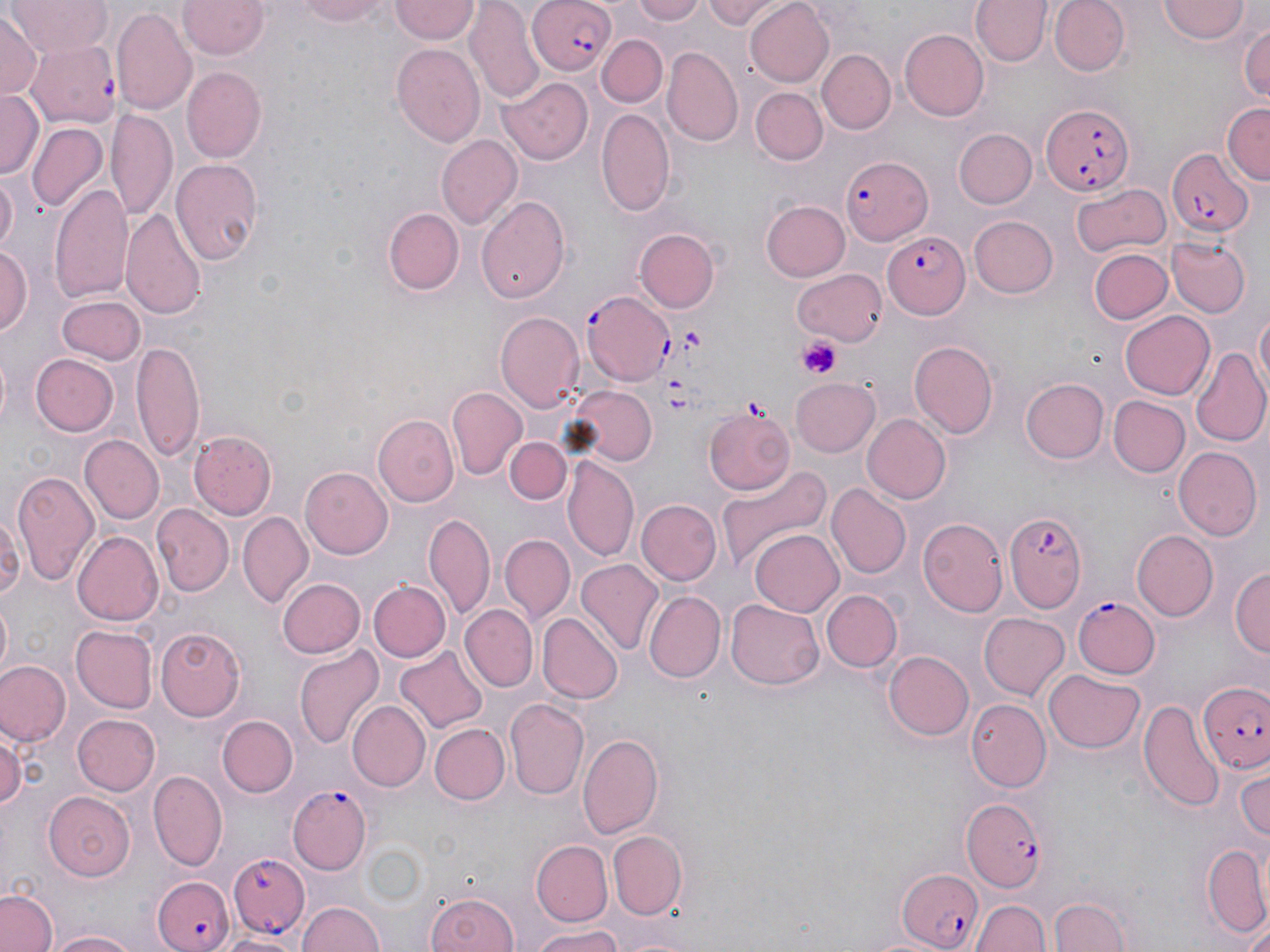

slide-level diagnosis = Plasmodium falciparum
preparation = thin blood smear
stain = May-Grünwald-Giemsa
platelet locations = approximate bounding boxes as [x1, y1, x2, y2] in pixels: [680, 325, 710, 356], [798, 338, 841, 378], [740, 394, 769, 415]
modality = light microscopy
uninfected red blood cell locations = approximate bounding boxes as [x1, y1, x2, y2] in pixels: [7, 0, 112, 59], [178, 0, 268, 58], [291, 0, 397, 26], [631, 0, 706, 24], [703, 0, 778, 31], [969, 0, 1049, 67], [1049, 0, 1129, 74], [390, 1, 479, 43], [743, 1, 835, 88], [1158, 1, 1248, 44], [465, 5, 545, 101], [111, 9, 196, 116], [0, 11, 41, 100], [1238, 18, 1270, 107], [898, 28, 989, 121], [596, 34, 667, 107], [390, 40, 484, 144], [663, 48, 743, 145], [819, 50, 895, 134], [183, 66, 265, 163], [499, 76, 592, 164], [750, 87, 827, 166], [1, 91, 42, 177], [1222, 103, 1270, 184], [595, 106, 676, 218], [108, 108, 177, 222], [26, 122, 107, 214], [952, 129, 1036, 209], [438, 135, 522, 228], [170, 159, 263, 266], [1, 174, 18, 260], [1071, 181, 1171, 262], [49, 183, 134, 302], [476, 193, 571, 305], [761, 200, 851, 281], [122, 207, 207, 322], [383, 208, 463, 295], [970, 216, 1059, 298], [634, 228, 718, 313], [1169, 235, 1251, 316], [0, 244, 31, 340], [1090, 248, 1172, 325], [792, 268, 888, 344], [57, 298, 146, 365], [495, 309, 584, 410], [1254, 309, 1270, 401], [1121, 312, 1215, 399], [132, 336, 205, 465], [910, 340, 998, 437], [1192, 346, 1270, 445], [29, 353, 119, 437], [791, 376, 881, 455], [1023, 378, 1108, 463], [566, 386, 657, 469], [447, 389, 526, 480], [1108, 396, 1189, 477], [704, 407, 796, 496], [375, 413, 457, 506], [863, 415, 950, 502], [189, 430, 277, 517], [79, 434, 164, 524], [504, 437, 571, 505], [1173, 446, 1260, 539], [562, 454, 638, 563], [717, 465, 833, 569], [301, 466, 394, 557], [11, 468, 99, 583], [826, 485, 909, 579], [637, 501, 719, 584], [152, 505, 233, 595], [0, 510, 21, 605], [237, 513, 313, 606], [425, 515, 494, 616], [917, 518, 1007, 617], [750, 529, 844, 617], [73, 530, 164, 625], [1132, 531, 1218, 620], [499, 535, 573, 620], [576, 559, 664, 657], [1231, 565, 1269, 661], [277, 577, 366, 659], [369, 581, 449, 662], [646, 589, 726, 682], [821, 590, 902, 671], [1, 597, 14, 677], [726, 598, 822, 691], [460, 604, 538, 690], [537, 613, 621, 703], [979, 613, 1070, 700], [155, 625, 247, 719], [72, 626, 158, 713], [295, 644, 384, 751], [395, 646, 488, 735], [883, 650, 973, 740], [0, 661, 70, 747], [1045, 668, 1144, 753], [967, 698, 1052, 792], [1140, 698, 1226, 814], [505, 699, 589, 801], [348, 700, 429, 789], [73, 713, 161, 797], [218, 714, 298, 798], [429, 723, 508, 805], [0, 730, 22, 815], [576, 730, 668, 840], [1235, 765, 1270, 843], [148, 768, 226, 869], [44, 791, 136, 880], [608, 829, 687, 918], [533, 842, 613, 926], [1198, 842, 1270, 944], [422, 887, 522, 952], [0, 888, 59, 952], [1044, 893, 1133, 951], [297, 898, 384, 952], [974, 898, 1049, 952], [529, 927, 631, 952], [48, 930, 138, 952], [221, 930, 303, 952]
magnification = 1000x
image size = 1270×952 pixels
field of view = one of a larger specimen
Plasmodium falciparum-infected red blood cell locations = approximate bounding boxes as [x1, y1, x2, y2] in pixels: [527, 0, 616, 76], [29, 40, 119, 127], [1038, 102, 1135, 197], [1166, 146, 1253, 236], [842, 156, 933, 244], [883, 232, 968, 319], [582, 290, 677, 383], [1004, 509, 1086, 613], [1074, 596, 1160, 679], [1201, 681, 1270, 776], [288, 786, 371, 872], [963, 802, 1051, 893], [230, 852, 310, 935], [901, 870, 984, 951], [152, 873, 234, 952]